Name the blood parasite species.
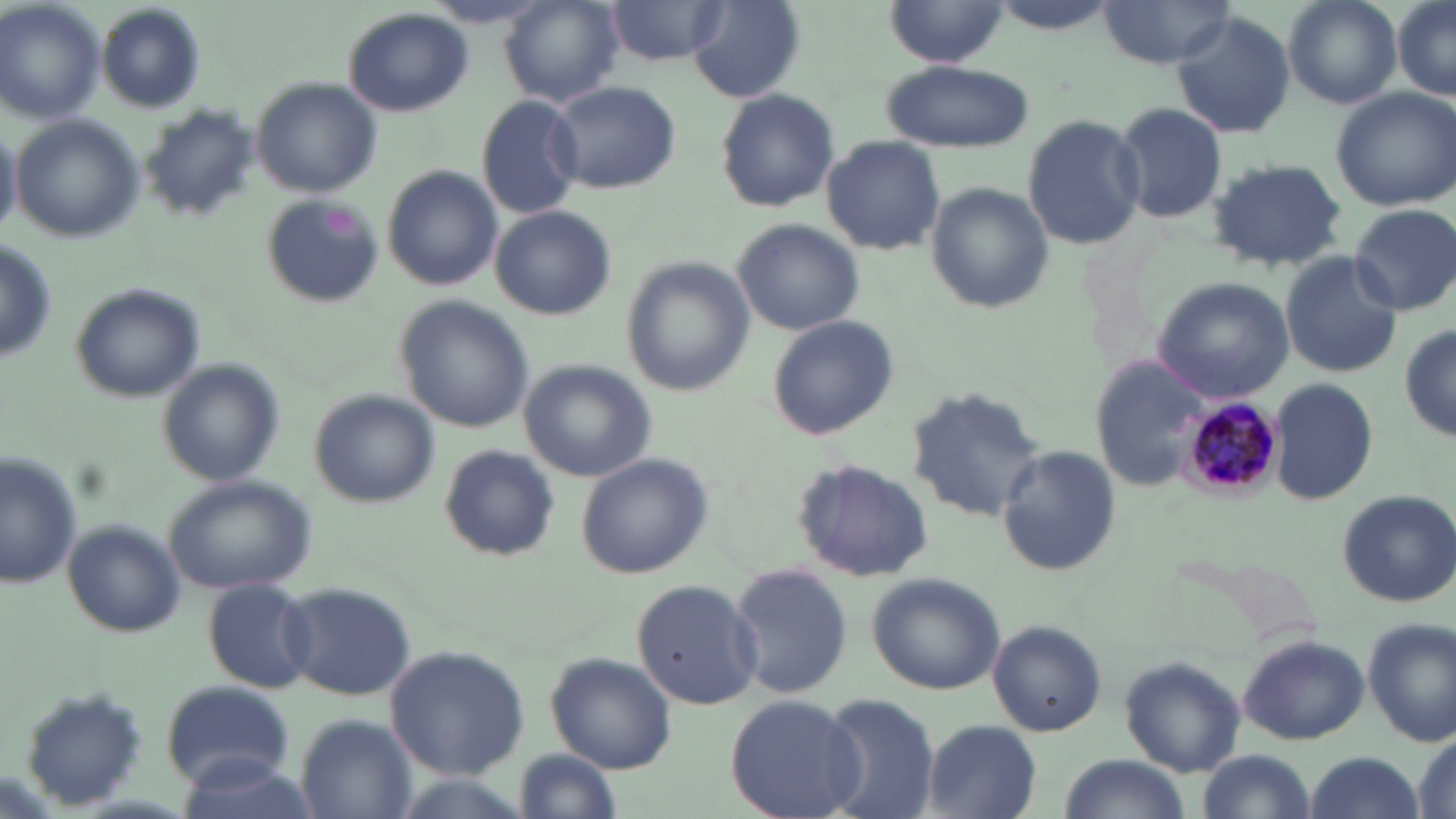

Plasmodium malariae.

Summary:
  - Coordinate format: approximate bounding boxes as (x1,y1)-(x2,y2) corner pairs in pixels
  - Platelet locations: (322,204)-(361,238)
  - Uninfected red blood cell locations: (501,0)-(625,107), (1280,0)-(1402,109), (1392,0)-(1456,100), (0,1)-(105,124), (607,1)-(727,65), (1094,1)-(1238,71), (423,2)-(555,30), (688,2)-(807,103), (882,3)-(1012,68), (97,4)-(207,112), (341,7)-(474,118), (1171,12)-(1297,138), (880,58)-(1035,153), (252,78)-(383,198), (546,80)-(681,195), (1330,87)-(1456,209), (714,88)-(841,212), (476,95)-(585,219), (1110,100)-(1230,225), (140,105)-(259,222), (1022,112)-(1144,250), (9,115)-(146,243), (0,120)-(21,238), (822,136)-(945,254), (1205,158)-(1349,273), (381,165)-(503,292), (926,183)-(1058,313), (260,196)-(383,308), (490,204)-(617,320), (1348,204)-(1456,315), (732,216)-(866,335), (1279,250)-(1402,379), (619,256)-(753,399), (1153,277)-(1294,401), (69,283)-(205,402), (396,297)-(537,433), (766,315)-(898,441), (1399,321)-(1455,446), (156,358)-(284,486), (1091,358)-(1208,488), (519,360)-(659,482), (1269,377)-(1380,506), (907,385)-(1049,520), (311,390)-(441,507), (995,443)-(1122,578), (440,445)-(559,561), (0,447)-(79,585), (575,453)-(714,580), (792,459)-(936,583), (162,475)-(318,596), (1335,487)-(1456,607), (61,520)-(186,639), (729,560)-(851,700), (867,571)-(1006,694), (631,577)-(766,710), (204,580)-(322,693), (281,580)-(414,701), (1363,618)-(1455,746), (989,621)-(1106,736), (1236,635)-(1367,744), (385,645)-(528,780), (546,652)-(677,772), (1120,657)-(1246,777), (159,679)-(293,789), (17,687)-(148,810), (724,692)-(863,819), (814,692)-(941,819), (294,714)-(413,817), (921,720)-(1041,818), (1410,726)-(1454,818), (509,745)-(625,819), (1196,749)-(1318,819), (1302,751)-(1424,819), (172,753)-(320,819), (1055,754)-(1193,819)
  - Plasmodium malariae-infected red blood cell locations: (1178,398)-(1283,503)
  - Preparation: thin blood film
  - Stain: May-Grünwald-Giemsa
  - Modality: optical microscopy
  - Magnification: 1000x
  - Field of view: single
  - Image size: 1456×819 pixels